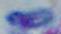
modality: photomicrograph
identification: Toxoplasma gondii
magnification: 1000x